Assess this cell for malaria.
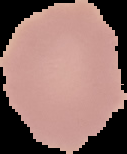

Uninfected.

From a thin blood smear. Cell region segmented out of the field of view; the surrounding area is masked to black. Image is 127×154 pixels.